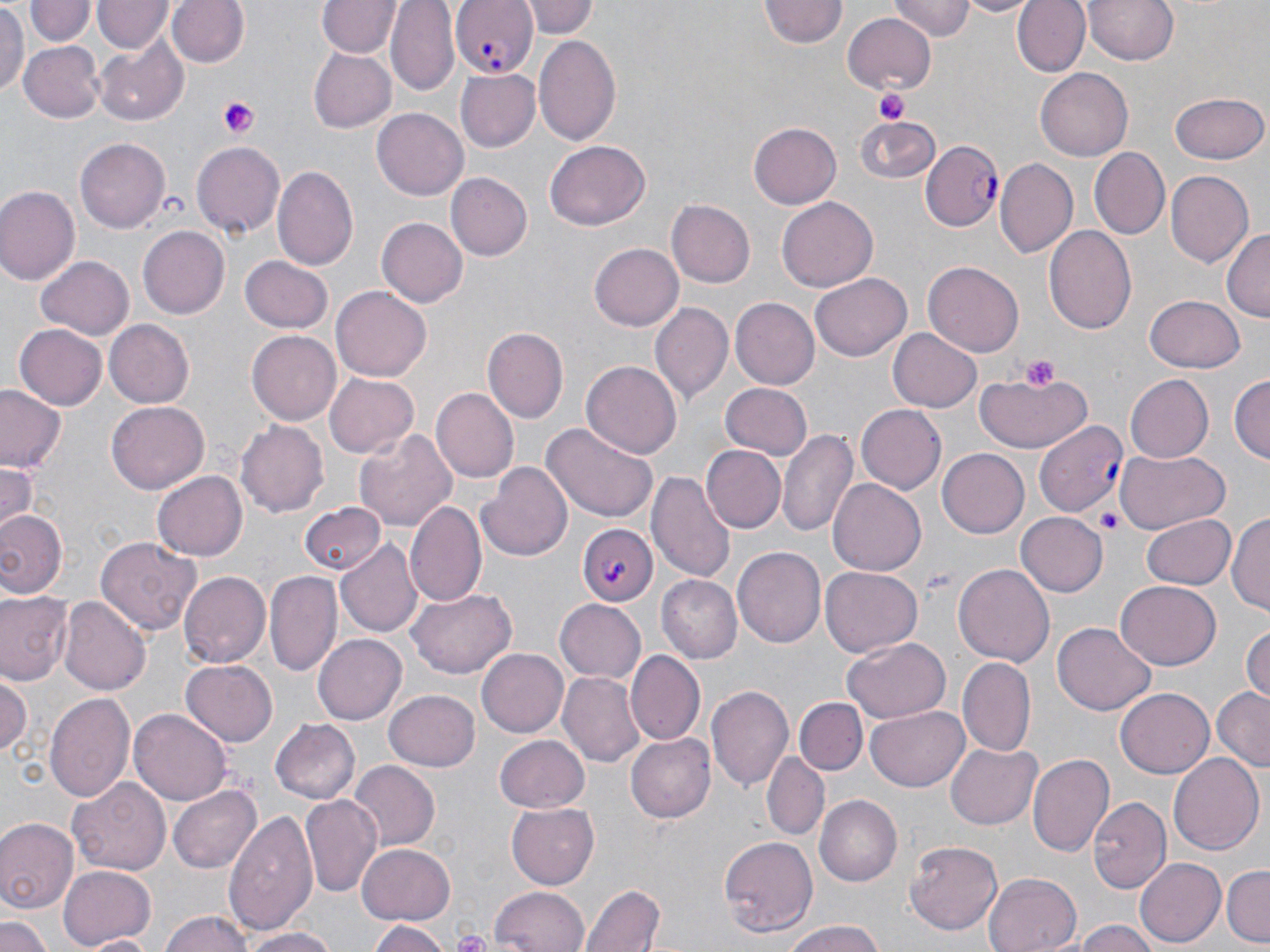 Approximate bounding boxes as named x1/y1/x2/y2 corners in pixels. Uninfected red blood cell locations: (x1=169, y1=0, x2=248, y2=69), (x1=528, y1=0, x2=599, y2=38), (x1=761, y1=0, x2=845, y2=50), (x1=889, y1=0, x2=974, y2=39), (x1=958, y1=0, x2=1037, y2=16), (x1=1013, y1=0, x2=1091, y2=77), (x1=1082, y1=0, x2=1183, y2=66), (x1=28, y1=1, x2=96, y2=47), (x1=95, y1=1, x2=172, y2=52), (x1=319, y1=1, x2=399, y2=59), (x1=386, y1=1, x2=459, y2=93), (x1=0, y1=2, x2=27, y2=95), (x1=842, y1=11, x2=938, y2=94), (x1=533, y1=34, x2=623, y2=148), (x1=95, y1=40, x2=187, y2=124), (x1=20, y1=41, x2=105, y2=122), (x1=310, y1=50, x2=395, y2=131), (x1=455, y1=68, x2=540, y2=151), (x1=1035, y1=69, x2=1134, y2=162), (x1=1172, y1=91, x2=1267, y2=164), (x1=372, y1=108, x2=468, y2=200), (x1=855, y1=114, x2=940, y2=185), (x1=748, y1=122, x2=841, y2=209), (x1=75, y1=137, x2=171, y2=234), (x1=542, y1=140, x2=650, y2=229), (x1=192, y1=141, x2=287, y2=237), (x1=1090, y1=147, x2=1170, y2=239), (x1=995, y1=159, x2=1078, y2=258), (x1=273, y1=166, x2=357, y2=273), (x1=1167, y1=171, x2=1253, y2=267), (x1=445, y1=172, x2=531, y2=262), (x1=0, y1=185, x2=79, y2=285), (x1=777, y1=196, x2=878, y2=290), (x1=666, y1=199, x2=754, y2=288), (x1=376, y1=217, x2=468, y2=309), (x1=137, y1=223, x2=229, y2=318), (x1=1043, y1=226, x2=1137, y2=337), (x1=1220, y1=227, x2=1269, y2=323), (x1=588, y1=240, x2=684, y2=333), (x1=37, y1=256, x2=134, y2=341), (x1=238, y1=256, x2=332, y2=334), (x1=923, y1=260, x2=1025, y2=356), (x1=811, y1=273, x2=912, y2=362), (x1=332, y1=286, x2=432, y2=380), (x1=1146, y1=297, x2=1245, y2=373), (x1=730, y1=298, x2=818, y2=389), (x1=649, y1=302, x2=733, y2=405), (x1=104, y1=318, x2=193, y2=406), (x1=13, y1=324, x2=107, y2=409), (x1=889, y1=326, x2=982, y2=412), (x1=485, y1=327, x2=568, y2=423), (x1=247, y1=331, x2=340, y2=426), (x1=580, y1=361, x2=682, y2=459), (x1=972, y1=369, x2=1096, y2=453), (x1=325, y1=371, x2=419, y2=456), (x1=1230, y1=374, x2=1268, y2=466), (x1=1123, y1=375, x2=1214, y2=464), (x1=720, y1=383, x2=813, y2=461), (x1=0, y1=386, x2=67, y2=472), (x1=433, y1=387, x2=521, y2=483), (x1=107, y1=401, x2=209, y2=493), (x1=857, y1=407, x2=945, y2=494), (x1=237, y1=419, x2=331, y2=516), (x1=539, y1=422, x2=660, y2=524), (x1=355, y1=427, x2=457, y2=531), (x1=778, y1=429, x2=860, y2=540), (x1=700, y1=445, x2=786, y2=533), (x1=1113, y1=449, x2=1229, y2=534), (x1=938, y1=450, x2=1028, y2=537), (x1=0, y1=462, x2=37, y2=534), (x1=477, y1=463, x2=575, y2=562), (x1=648, y1=470, x2=736, y2=582), (x1=152, y1=471, x2=247, y2=561), (x1=829, y1=479, x2=926, y2=576), (x1=408, y1=500, x2=485, y2=605), (x1=299, y1=502, x2=386, y2=576), (x1=0, y1=508, x2=66, y2=600), (x1=1230, y1=511, x2=1270, y2=621), (x1=1016, y1=513, x2=1106, y2=596), (x1=1140, y1=513, x2=1235, y2=589), (x1=95, y1=536, x2=202, y2=638), (x1=337, y1=538, x2=422, y2=637), (x1=735, y1=546, x2=827, y2=648), (x1=954, y1=563, x2=1054, y2=668), (x1=818, y1=567, x2=923, y2=656), (x1=178, y1=570, x2=272, y2=669), (x1=265, y1=570, x2=343, y2=677), (x1=659, y1=575, x2=742, y2=662), (x1=1114, y1=582, x2=1221, y2=669), (x1=409, y1=588, x2=517, y2=679), (x1=1, y1=592, x2=71, y2=686), (x1=60, y1=597, x2=150, y2=695), (x1=554, y1=599, x2=646, y2=682), (x1=1052, y1=622, x2=1156, y2=715), (x1=1242, y1=623, x2=1270, y2=706), (x1=312, y1=634, x2=406, y2=726), (x1=842, y1=639, x2=951, y2=722), (x1=477, y1=647, x2=572, y2=737), (x1=626, y1=651, x2=704, y2=743), (x1=958, y1=657, x2=1036, y2=758), (x1=181, y1=659, x2=279, y2=745), (x1=557, y1=670, x2=644, y2=766), (x1=0, y1=674, x2=31, y2=760), (x1=707, y1=684, x2=795, y2=795), (x1=1210, y1=687, x2=1270, y2=768), (x1=387, y1=689, x2=480, y2=770), (x1=1116, y1=689, x2=1214, y2=778), (x1=45, y1=692, x2=135, y2=802), (x1=797, y1=698, x2=867, y2=773), (x1=866, y1=707, x2=969, y2=790), (x1=131, y1=708, x2=232, y2=807), (x1=270, y1=718, x2=360, y2=804), (x1=626, y1=732, x2=716, y2=822), (x1=494, y1=735, x2=590, y2=813), (x1=947, y1=741, x2=1041, y2=828), (x1=1167, y1=752, x2=1265, y2=858), (x1=762, y1=753, x2=829, y2=841), (x1=1028, y1=753, x2=1116, y2=859), (x1=348, y1=763, x2=438, y2=851), (x1=69, y1=775, x2=171, y2=872), (x1=169, y1=784, x2=261, y2=873), (x1=301, y1=795, x2=383, y2=898), (x1=816, y1=797, x2=902, y2=885), (x1=1089, y1=798, x2=1175, y2=894), (x1=506, y1=804, x2=599, y2=889), (x1=223, y1=812, x2=318, y2=936), (x1=0, y1=818, x2=78, y2=917), (x1=720, y1=836, x2=818, y2=939), (x1=905, y1=840, x2=1003, y2=935), (x1=355, y1=842, x2=457, y2=924), (x1=1135, y1=857, x2=1226, y2=947), (x1=58, y1=865, x2=156, y2=949), (x1=1222, y1=865, x2=1270, y2=944), (x1=982, y1=872, x2=1083, y2=952), (x1=581, y1=885, x2=665, y2=952), (x1=489, y1=886, x2=589, y2=952), (x1=160, y1=911, x2=256, y2=952), (x1=0, y1=917, x2=52, y2=952), (x1=366, y1=918, x2=449, y2=951), (x1=1074, y1=921, x2=1164, y2=952), (x1=778, y1=923, x2=890, y2=952), (x1=236, y1=927, x2=344, y2=952), (x1=79, y1=933, x2=158, y2=951). Platelet locations: (x1=876, y1=88, x2=910, y2=125), (x1=217, y1=96, x2=261, y2=140), (x1=1019, y1=354, x2=1062, y2=388), (x1=1095, y1=504, x2=1125, y2=535). Plasmodium falciparum-infected red blood cell locations: (x1=448, y1=0, x2=537, y2=78), (x1=920, y1=141, x2=1003, y2=232), (x1=1034, y1=420, x2=1129, y2=518), (x1=578, y1=523, x2=656, y2=605). Slide-level diagnosis: Plasmodium falciparum. Image is 1270×952 pixels. One field of a larger specimen. May-Grünwald-Giemsa-stained preparation. Thin blood smear. Optical microscopy. 1000x magnification.